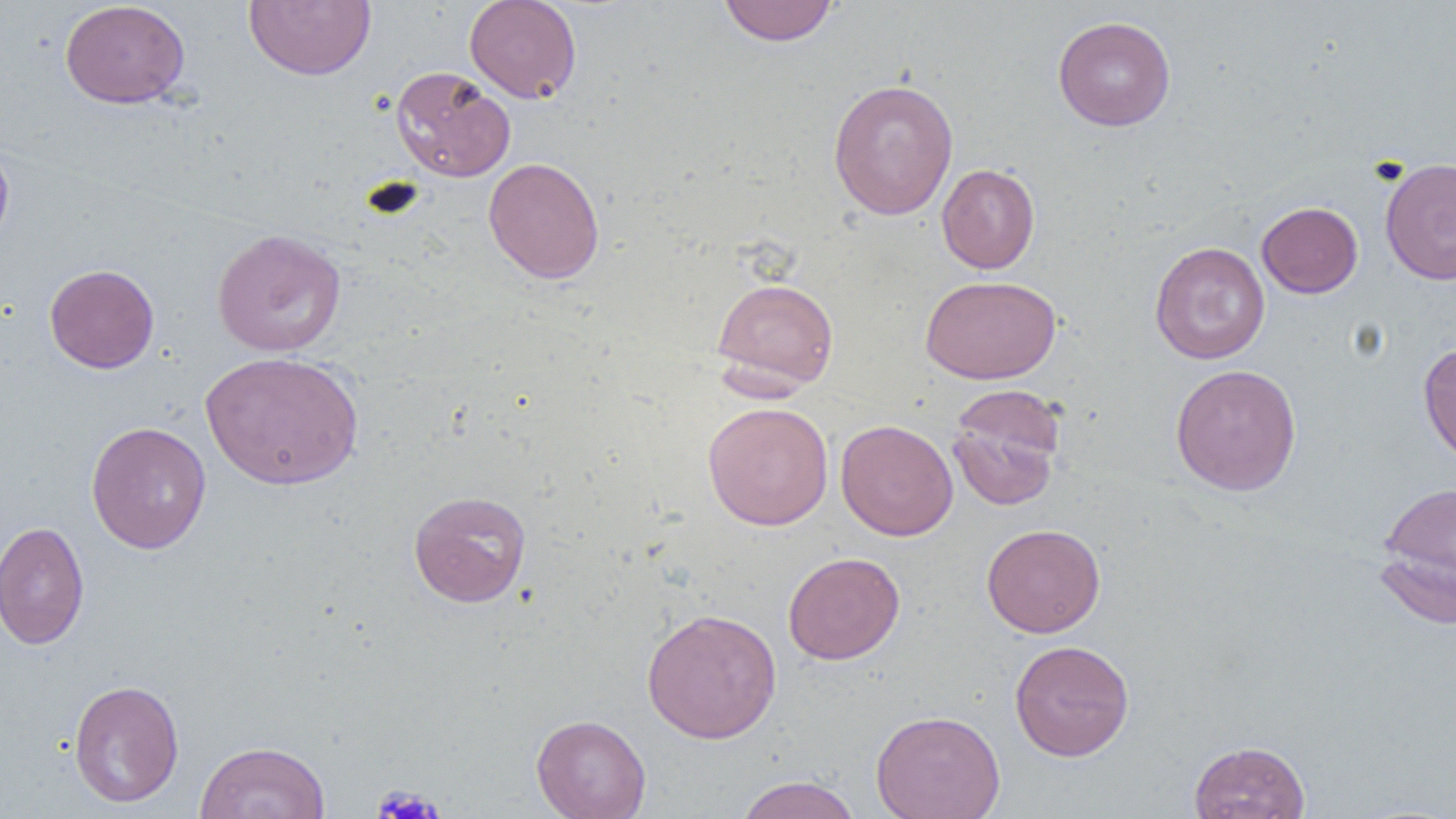
Approximate bounding boxes as (x1,y1)-(x2,y2) corner pairs in pixels. Platelet locations: (371,785)-(445,819). Uninfected red blood cell locations: (243,0)-(376,81), (463,0)-(582,103), (59,1)-(190,109), (718,1)-(838,46), (1052,15)-(1177,131), (389,65)-(516,182), (827,78)-(959,220), (0,139)-(14,253), (483,157)-(605,285), (1380,157)-(1456,285), (936,164)-(1040,273), (1256,202)-(1363,298), (211,228)-(347,357), (1149,241)-(1270,364), (44,263)-(159,373), (921,275)-(1060,384), (711,277)-(839,391), (1418,342)-(1456,466), (200,351)-(364,490), (1170,364)-(1302,496), (946,386)-(1066,511), (702,401)-(833,530), (835,419)-(958,541), (85,421)-(212,554), (1378,480)-(1456,613), (408,490)-(531,607), (0,521)-(90,650), (981,523)-(1106,638), (783,551)-(905,664), (641,608)-(782,744), (1009,639)-(1134,761), (68,679)-(184,807), (870,709)-(1005,819), (531,714)-(651,819), (1188,740)-(1310,819), (194,741)-(330,819), (734,775)-(863,819). Slide-level diagnosis: negative for blood parasites. Optical microscopy. Image is 1456×819 pixels. Thin blood smear. Captured at 1000x magnification. One field of a larger specimen.